Name the parasite shown.
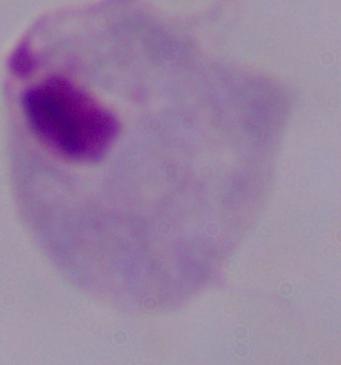

This is a trichomonad.

Photomicrograph. 1000x magnification.